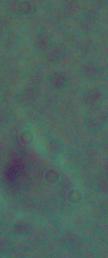
Photomicrograph. 1000x magnification. A Leishmania parasite is shown.